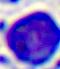
Summary:
  - Magnification: 400x
  - Identification: white blood cell
  - Modality: photomicrograph